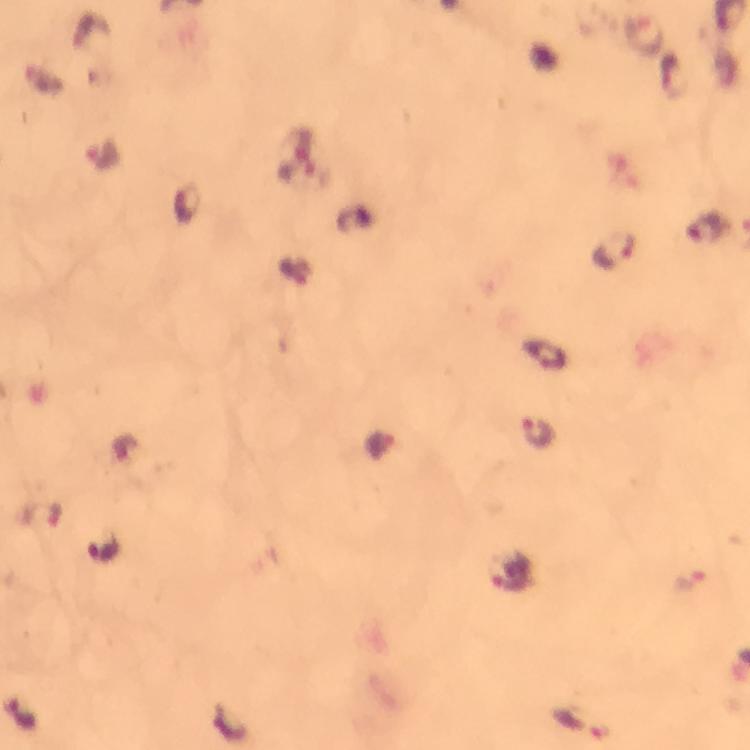
immersion oil = applied
stain = Giemsa
image size = 750×750 pixels
cropped from = one field of view
capture = smartphone mounted on the microscope
context = from a diagnostic examination for malaria
Plasmodium parasite locations = approximate centers as {x, y} in pixels: {640, 36}, {103, 153}, {707, 227}, {613, 249}, {545, 353}, {539, 432}, {105, 550}, {511, 571}, {693, 580}, {581, 724}
preparation = thick blood film
magnification = 100x